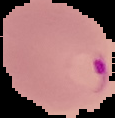
preparation = thin blood smear
result = malaria parasites detected
image size = 115×118 pixels
image type = segmented cell region with the area outside set to black